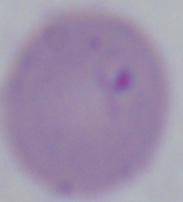
Summary:
  - Identification: Babesia
  - Magnification: 1000x
  - Modality: micrograph